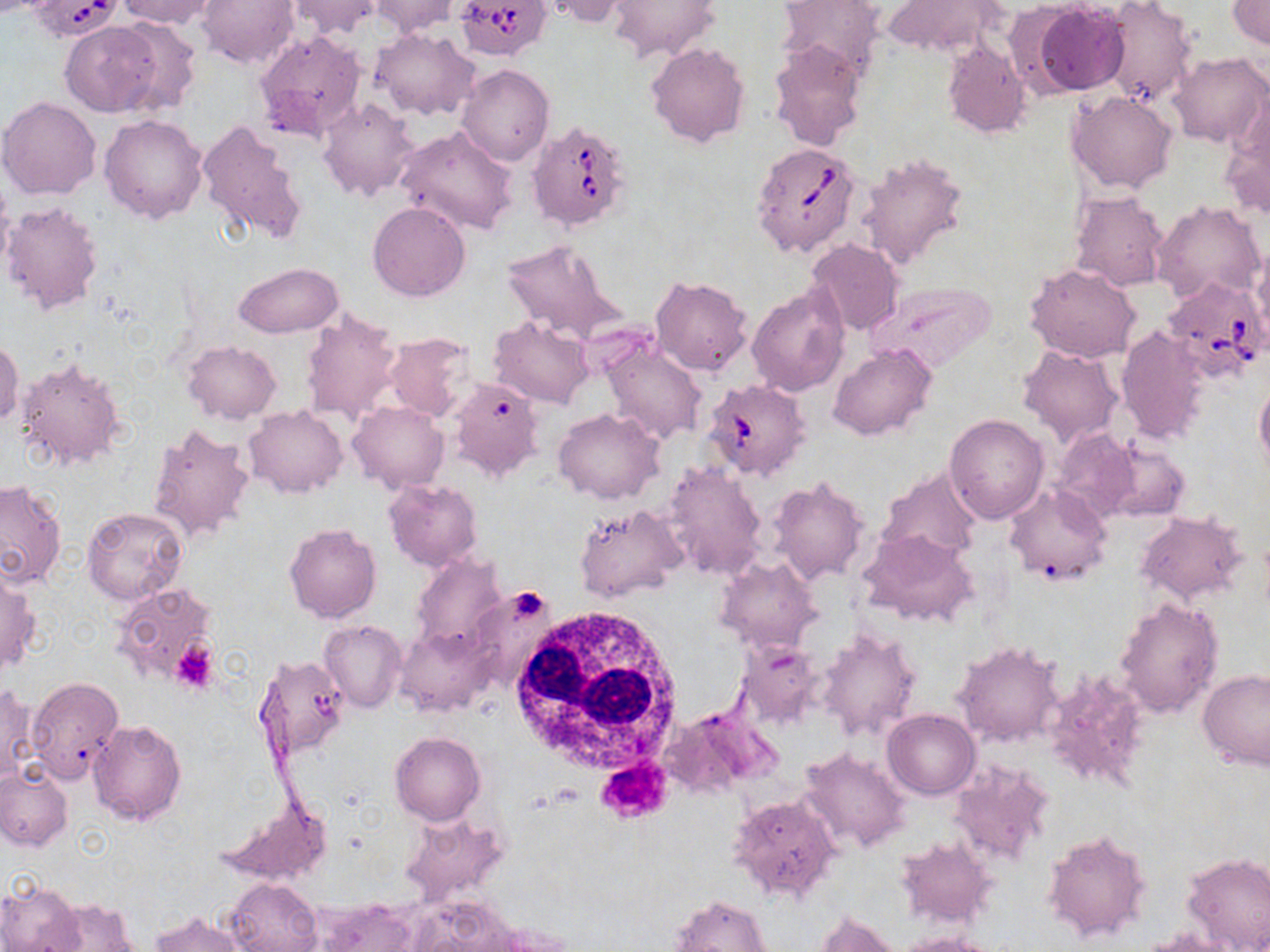

Approximate bounding boxes as named x1/y1/x2/y2 corners in pixels. Uninfected red blood cell locations: (x1=115, y1=0, x2=219, y2=29), (x1=198, y1=0, x2=299, y2=70), (x1=284, y1=0, x2=383, y2=39), (x1=368, y1=0, x2=458, y2=37), (x1=536, y1=0, x2=637, y2=26), (x1=776, y1=0, x2=885, y2=76), (x1=1227, y1=0, x2=1270, y2=49), (x1=608, y1=1, x2=717, y2=60), (x1=884, y1=1, x2=1001, y2=58), (x1=1099, y1=1, x2=1197, y2=107), (x1=1028, y1=4, x2=1129, y2=96), (x1=108, y1=16, x2=202, y2=116), (x1=62, y1=21, x2=163, y2=117), (x1=372, y1=28, x2=479, y2=121), (x1=254, y1=31, x2=367, y2=141), (x1=943, y1=39, x2=1031, y2=139), (x1=768, y1=40, x2=866, y2=151), (x1=646, y1=42, x2=752, y2=148), (x1=1168, y1=52, x2=1268, y2=148), (x1=457, y1=64, x2=554, y2=166), (x1=1067, y1=89, x2=1176, y2=193), (x1=319, y1=96, x2=419, y2=201), (x1=1, y1=97, x2=101, y2=200), (x1=1222, y1=99, x2=1270, y2=222), (x1=7, y1=105, x2=205, y2=208), (x1=100, y1=115, x2=208, y2=224), (x1=199, y1=118, x2=309, y2=249), (x1=395, y1=127, x2=518, y2=236), (x1=857, y1=151, x2=968, y2=270), (x1=1069, y1=191, x2=1170, y2=292), (x1=1151, y1=200, x2=1267, y2=306), (x1=2, y1=201, x2=104, y2=315), (x1=368, y1=201, x2=470, y2=300), (x1=500, y1=239, x2=621, y2=344), (x1=807, y1=239, x2=903, y2=337), (x1=1251, y1=247, x2=1270, y2=349), (x1=234, y1=261, x2=343, y2=338), (x1=1026, y1=263, x2=1141, y2=363), (x1=651, y1=276, x2=751, y2=376), (x1=868, y1=282, x2=994, y2=373), (x1=748, y1=286, x2=847, y2=396), (x1=300, y1=306, x2=405, y2=427), (x1=489, y1=316, x2=593, y2=409), (x1=1116, y1=327, x2=1210, y2=444), (x1=383, y1=332, x2=480, y2=422), (x1=0, y1=336, x2=22, y2=431), (x1=600, y1=337, x2=708, y2=446), (x1=184, y1=341, x2=280, y2=423), (x1=830, y1=343, x2=935, y2=440), (x1=1018, y1=343, x2=1124, y2=445), (x1=16, y1=356, x2=129, y2=472), (x1=450, y1=376, x2=545, y2=479), (x1=1255, y1=379, x2=1270, y2=476), (x1=348, y1=401, x2=448, y2=491), (x1=245, y1=405, x2=346, y2=498), (x1=553, y1=408, x2=665, y2=503), (x1=945, y1=414, x2=1048, y2=525), (x1=146, y1=424, x2=255, y2=544), (x1=1081, y1=437, x2=1190, y2=524), (x1=663, y1=461, x2=766, y2=579), (x1=877, y1=468, x2=982, y2=566), (x1=767, y1=477, x2=871, y2=585), (x1=384, y1=478, x2=481, y2=570), (x1=0, y1=481, x2=65, y2=588), (x1=1004, y1=482, x2=1110, y2=585), (x1=574, y1=504, x2=687, y2=602), (x1=81, y1=507, x2=189, y2=607), (x1=1135, y1=512, x2=1247, y2=605), (x1=284, y1=523, x2=381, y2=622), (x1=857, y1=530, x2=979, y2=627), (x1=408, y1=555, x2=506, y2=655), (x1=716, y1=555, x2=824, y2=654), (x1=0, y1=569, x2=41, y2=677), (x1=113, y1=581, x2=217, y2=684), (x1=1114, y1=597, x2=1223, y2=721), (x1=319, y1=620, x2=407, y2=712), (x1=817, y1=625, x2=921, y2=741), (x1=399, y1=626, x2=493, y2=716), (x1=736, y1=639, x2=826, y2=727), (x1=954, y1=641, x2=1064, y2=747), (x1=259, y1=653, x2=351, y2=755), (x1=1041, y1=667, x2=1152, y2=791), (x1=1197, y1=670, x2=1270, y2=771), (x1=26, y1=677, x2=123, y2=784), (x1=0, y1=685, x2=37, y2=786), (x1=883, y1=708, x2=980, y2=799), (x1=88, y1=719, x2=185, y2=825), (x1=390, y1=731, x2=485, y2=825), (x1=796, y1=748, x2=911, y2=855), (x1=949, y1=760, x2=1055, y2=866), (x1=0, y1=764, x2=72, y2=851), (x1=219, y1=794, x2=327, y2=883), (x1=729, y1=794, x2=842, y2=902), (x1=1042, y1=829, x2=1153, y2=945), (x1=895, y1=837, x2=996, y2=929), (x1=1181, y1=851, x2=1270, y2=952), (x1=0, y1=877, x2=83, y2=951), (x1=228, y1=877, x2=320, y2=952), (x1=672, y1=894, x2=775, y2=952), (x1=41, y1=899, x2=141, y2=950), (x1=316, y1=899, x2=420, y2=952), (x1=150, y1=912, x2=244, y2=952), (x1=814, y1=912, x2=902, y2=952), (x1=898, y1=932, x2=999, y2=952). White blood cell locations: (x1=509, y1=604, x2=685, y2=779). Babesia divergens-infected red blood cell locations: (x1=455, y1=0, x2=552, y2=60), (x1=26, y1=1, x2=123, y2=38), (x1=528, y1=119, x2=634, y2=231), (x1=751, y1=141, x2=861, y2=258), (x1=1159, y1=276, x2=1267, y2=383), (x1=707, y1=380, x2=807, y2=488). Platelet locations: (x1=513, y1=587, x2=546, y2=619), (x1=172, y1=640, x2=218, y2=693), (x1=595, y1=756, x2=673, y2=824). Slide-level diagnosis: Babesia divergens. 1000x magnification. Image is 1270×952 pixels. Thin blood film. May-Grünwald-Giemsa stain. Light microscopy. One field of a larger specimen.